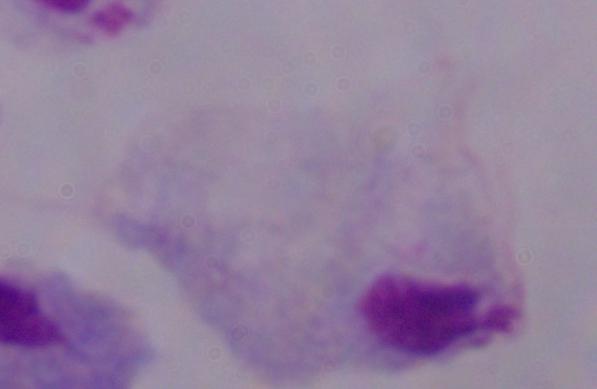

modality = photomicrograph
magnification = 1000x
identification = trichomonad